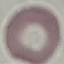

Malaria status: uninfected. Giemsa stain. Photographed with a smartphone camera at the microscope eyepiece. Thin blood smear. Automatically extracted cell patch, resized to 64 × 64 pixels.